Name the parasite shown.
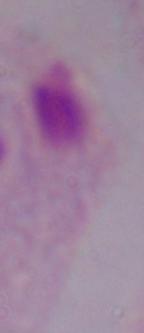

This is a trichomonad.

modality = photomicrograph
magnification = 1000x